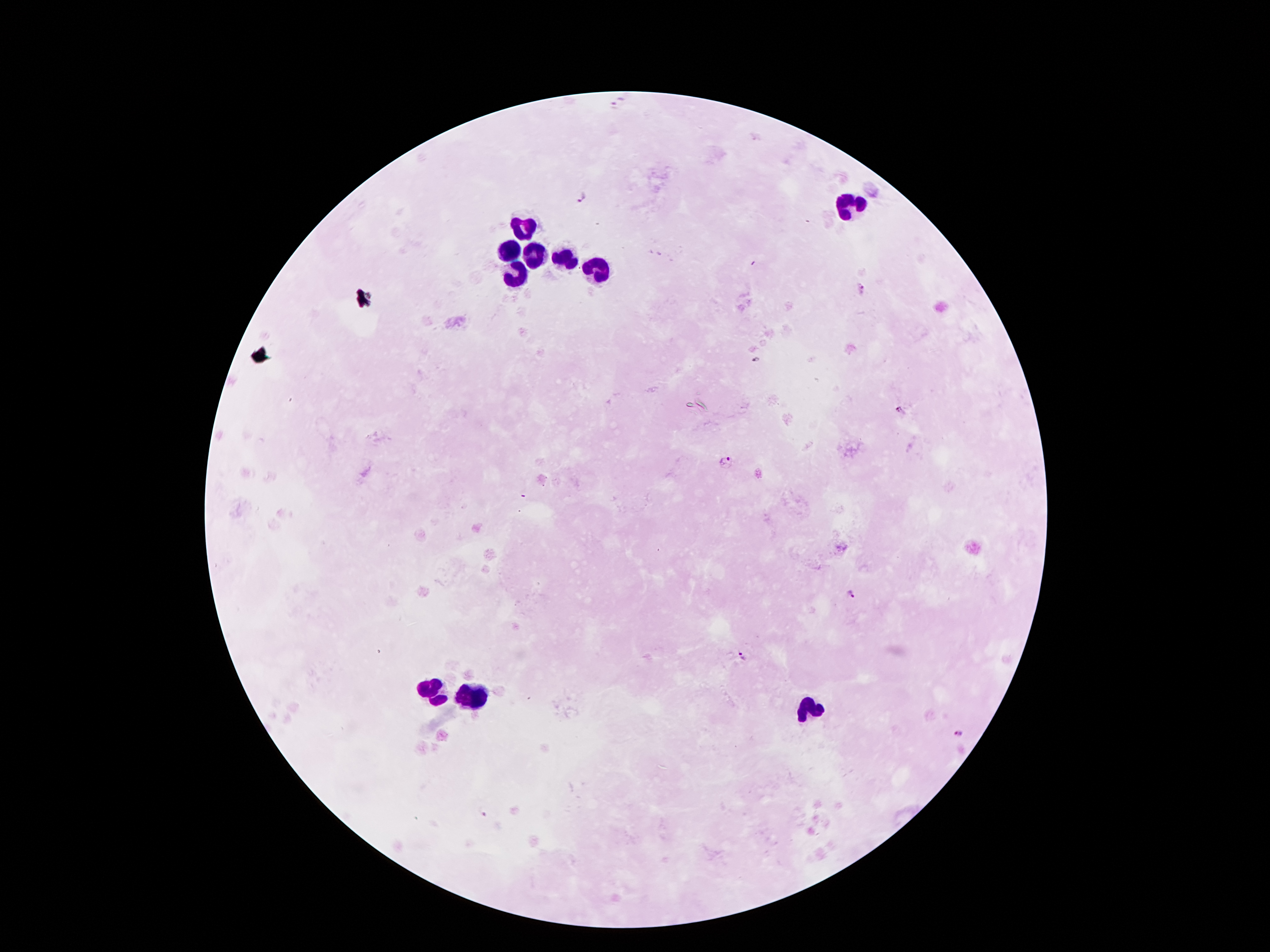
Approximate centers as [x, y] in pixels. Malaria parasite locations: [619, 100], [581, 195], [862, 289], [756, 362], [900, 411], [727, 461], [850, 594], [742, 656], [960, 733], [484, 812]. Leukocyte locations: [850, 206], [525, 229], [512, 249], [534, 252], [565, 257], [598, 270], [515, 272], [430, 690], [471, 698], [810, 713]. Patient malaria status: positive for Plasmodium falciparum. Smartphone photograph taken through the microscope eyepiece. 100x magnification. Image is 1270×952 pixels. One field from this slide. Thick peripheral-blood smear. Giemsa-stained preparation.